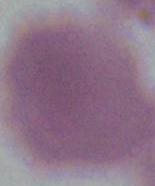
Summary:
  - Identification: red blood cell
  - Modality: micrograph
  - Magnification: 1000x